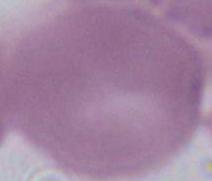
Summary:
  - Modality: photomicrograph
  - Magnification: 1000x
  - Identification: red blood cell